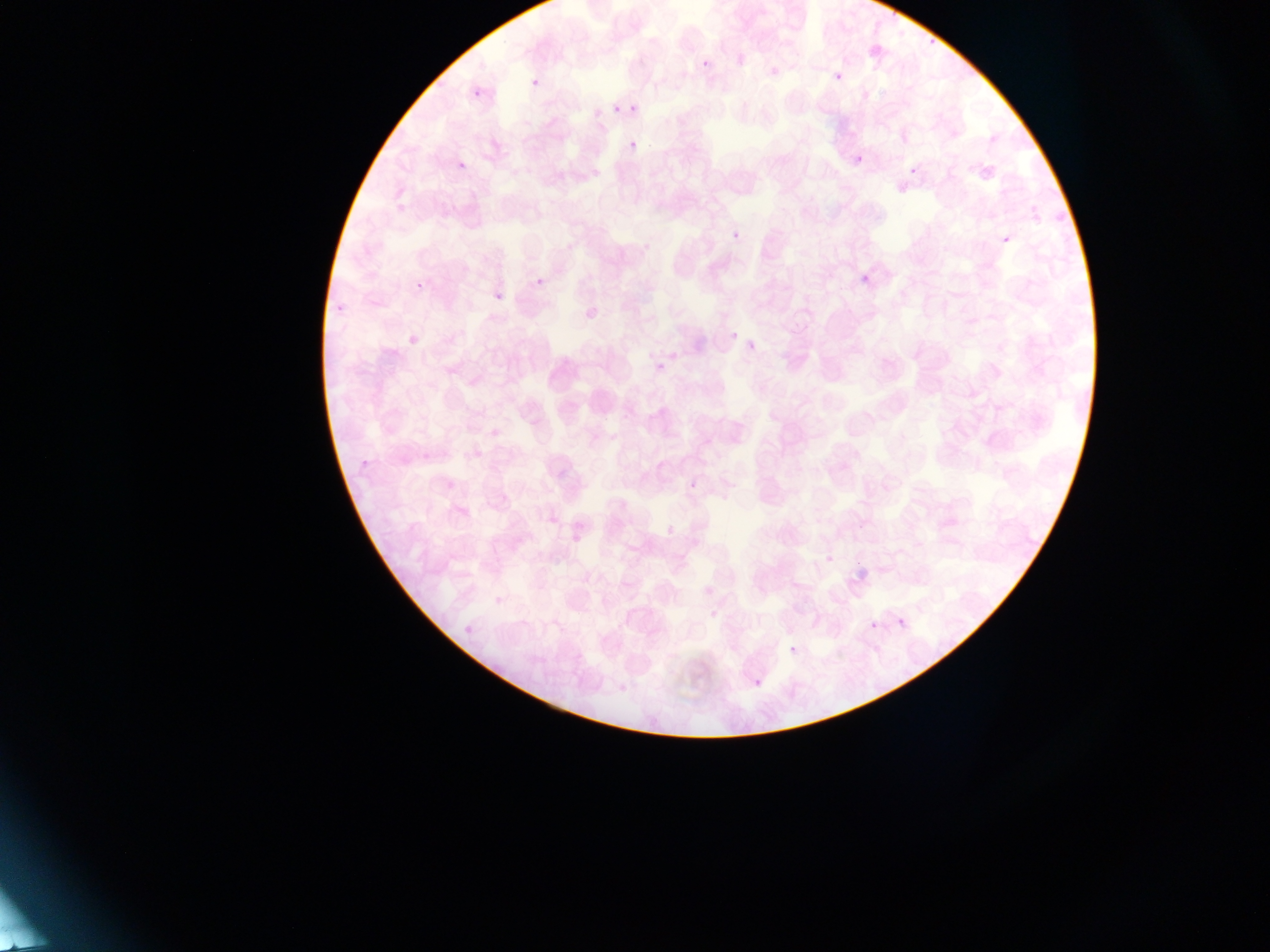

malaria parasite locations = approximate bounding boxes as [left, top, right, bottom] in pixels: [925, 30, 937, 48], [697, 56, 711, 68], [519, 68, 547, 94], [834, 72, 843, 81], [466, 91, 482, 103], [629, 101, 637, 114], [613, 105, 620, 113], [628, 140, 637, 150], [453, 144, 469, 171], [851, 148, 865, 170], [906, 160, 919, 175], [728, 223, 739, 242], [996, 235, 1013, 249], [532, 267, 548, 285], [854, 269, 877, 285], [413, 279, 425, 290], [490, 286, 504, 313], [329, 302, 347, 312], [725, 332, 739, 342], [746, 337, 760, 356], [664, 349, 687, 367], [650, 354, 666, 375], [357, 456, 371, 467], [691, 475, 703, 488], [664, 523, 675, 536], [819, 537, 837, 567], [852, 562, 873, 579], [490, 590, 507, 608], [896, 617, 905, 626], [460, 619, 474, 632], [869, 621, 880, 631], [789, 645, 797, 654], [750, 659, 764, 691], [617, 668, 631, 690]
capture = mobile-phone photograph through a microscope
field of view = single
country = Ghana
image size = 1270×952 pixels
preparation = thin blood film